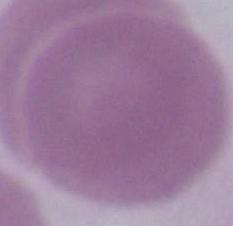

{
  "modality": "micrograph",
  "magnification": "1000x",
  "identification": "red blood cell"
}